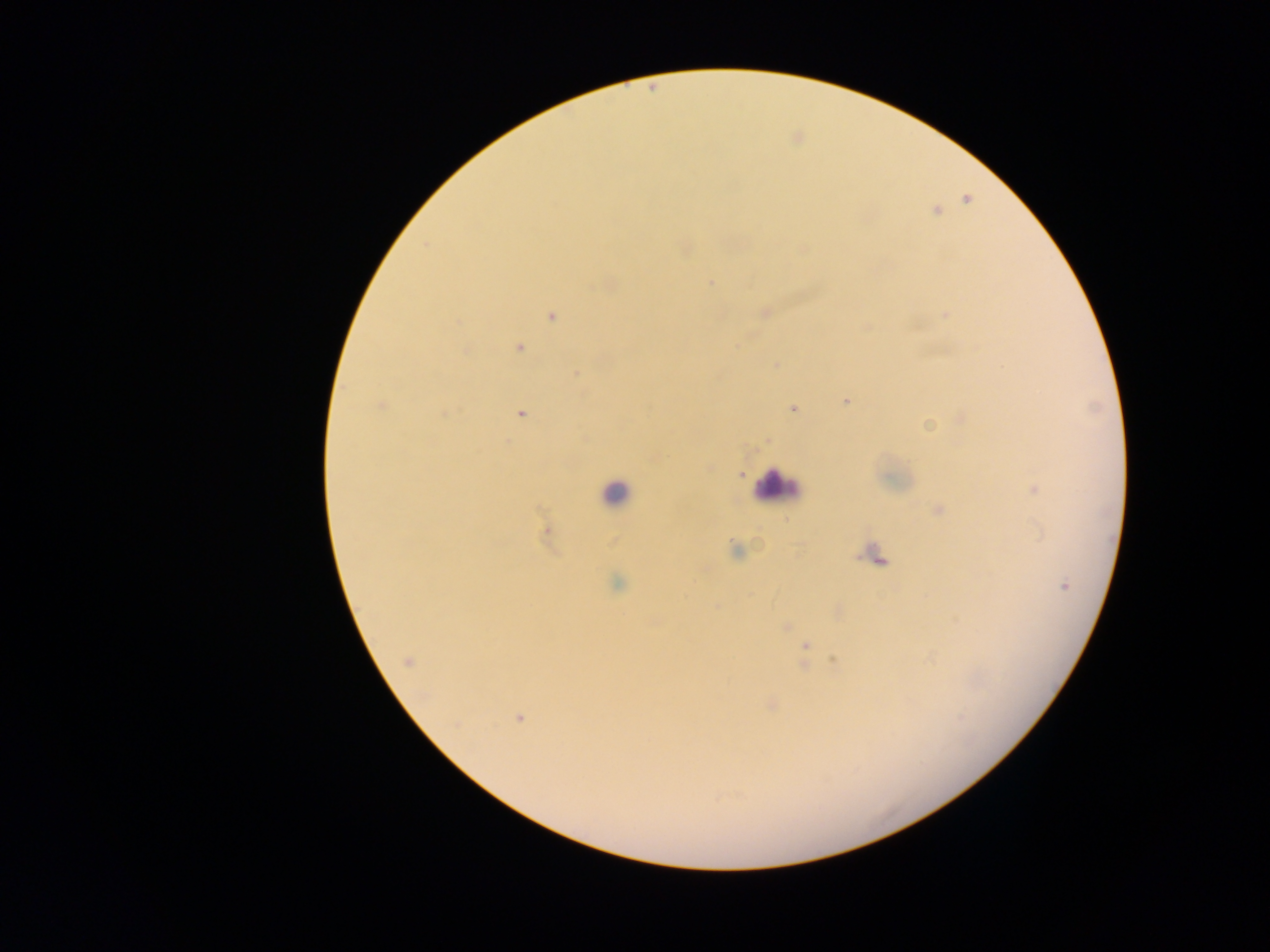 Approximate centers as (x, y) in pixels. Malaria parasite locations: (966, 199), (937, 211), (802, 249), (710, 282), (608, 284), (764, 313), (945, 314), (551, 315), (865, 327), (518, 347), (465, 350), (775, 365), (576, 374), (845, 400), (382, 406), (793, 407), (520, 414), (961, 419), (927, 423), (767, 439), (653, 457), (707, 468), (739, 473), (1034, 488), (938, 510), (547, 531), (736, 549), (876, 557), (617, 583), (1064, 585), (786, 627), (804, 647), (835, 660), (408, 661), (771, 705), (518, 717). Leukocyte locations: (777, 486), (615, 493). One field of view. Image is 1270×952 pixels. Mobile-phone photograph taken through the microscope. Thick blood film. Collected in Ghana.